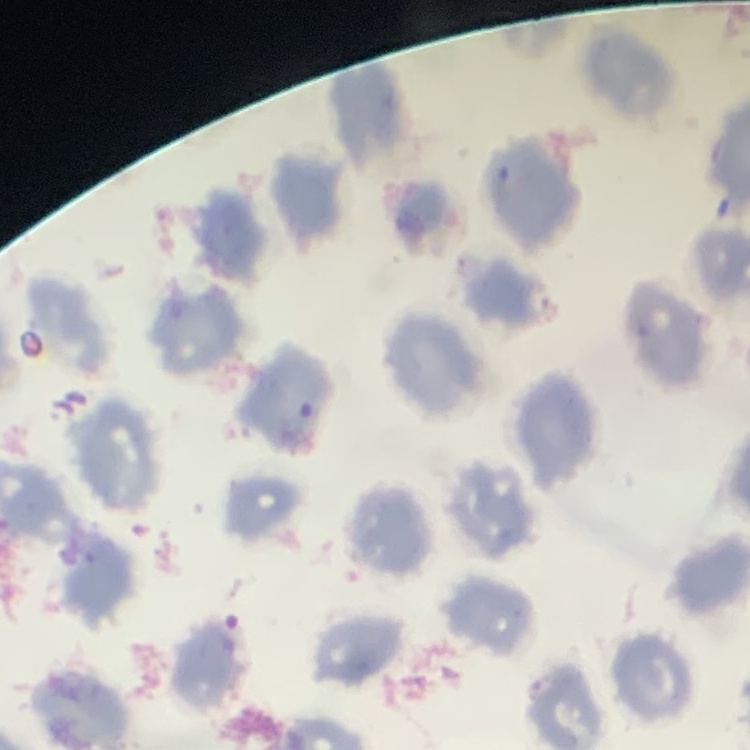

erythrocyte morphology = no rouleaux formation
stain = Field's or Giemsa
preparation = thin peripheral smear
image type = square crop of a larger photomicrograph